Point out each malaria parasite.
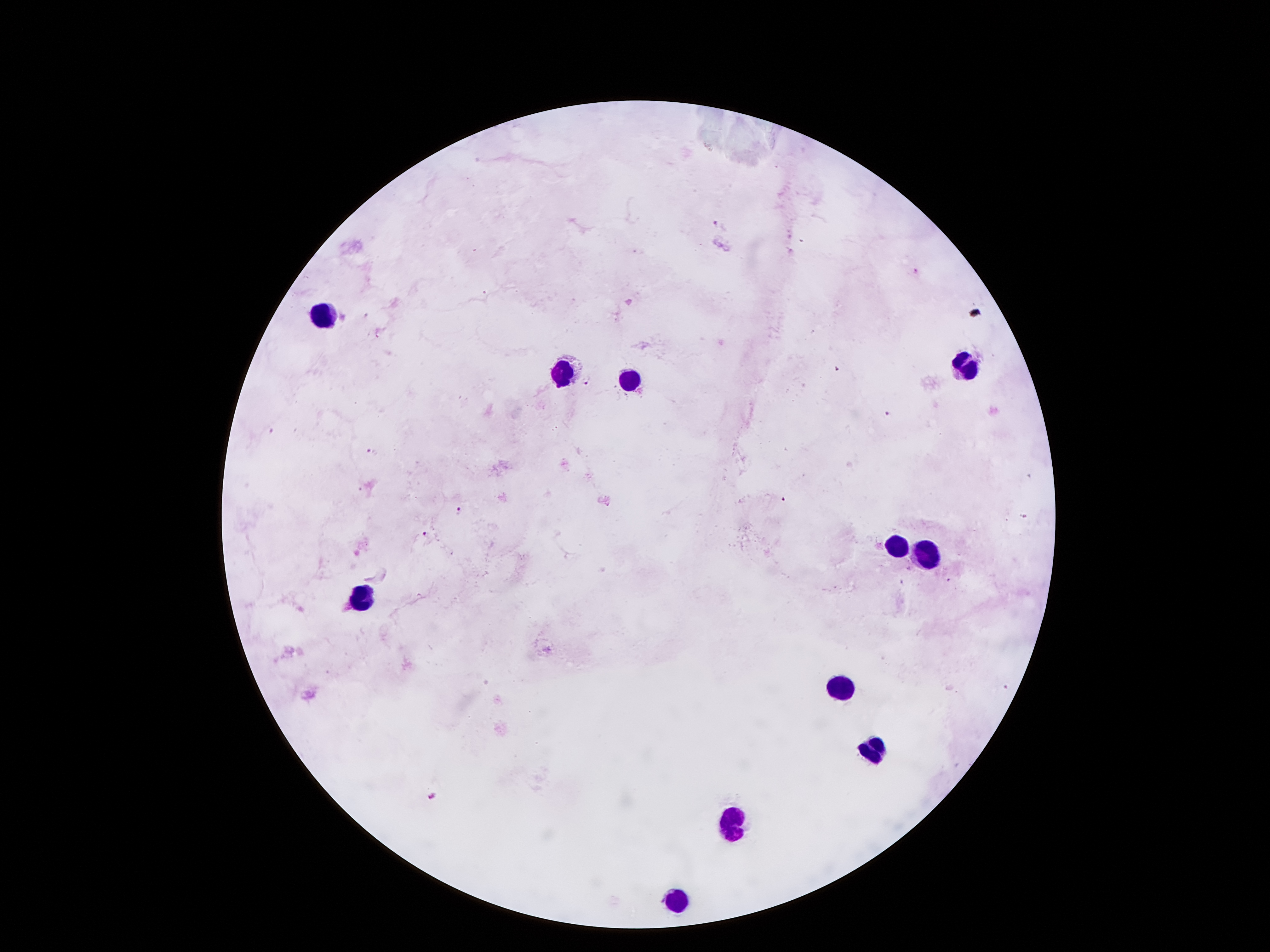
Approximate centers as [x, y] in pixels.
Malaria parasites: [719, 226], [915, 270], [367, 314], [838, 371], [587, 380], [889, 414], [271, 430], [371, 449], [786, 498], [459, 510], [425, 531], [434, 796].

Summary:
  - Leukocyte locations: [328, 316], [966, 368], [562, 373], [625, 377], [896, 546], [921, 552], [355, 592], [841, 689], [871, 751], [736, 823], [674, 903]
  - Field of view: single
  - Capture: smartphone camera through the microscope eyepiece
  - Preparation: thick blood film
  - Image size: 1270×952 pixels
  - Patient malaria status: infected with Plasmodium falciparum
  - Magnification: 100x
  - Stain: Giemsa